Classify this cell by malaria status.
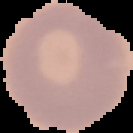
It is uninfected.

From a thin blood film. Image is 133×133 pixels. Segmented cell region on a black background.